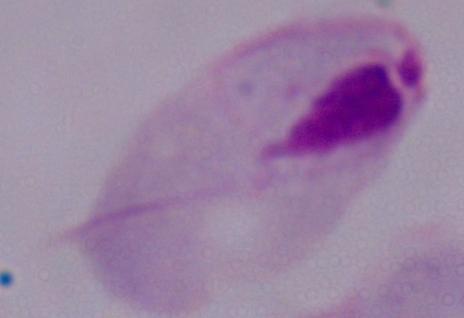

Summary:
  - Identification: trichomonad
  - Modality: micrograph
  - Magnification: 1000x